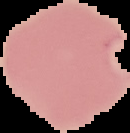
Summary:
  - Preparation: thin blood film
  - Result: malaria parasites identified
  - Image type: cell region segmented out of the field of view; surrounding area masked to black
  - Image size: 130×133 pixels